Classify this cell by malaria status.
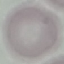
Uninfected.

Summary:
  - Stain: Giemsa
  - Preparation: thin blood smear
  - Capture: smartphone camera at the microscope eyepiece
  - Image type: cell patch, automatically extracted from a larger field of view and resized to 64 × 64 pixels